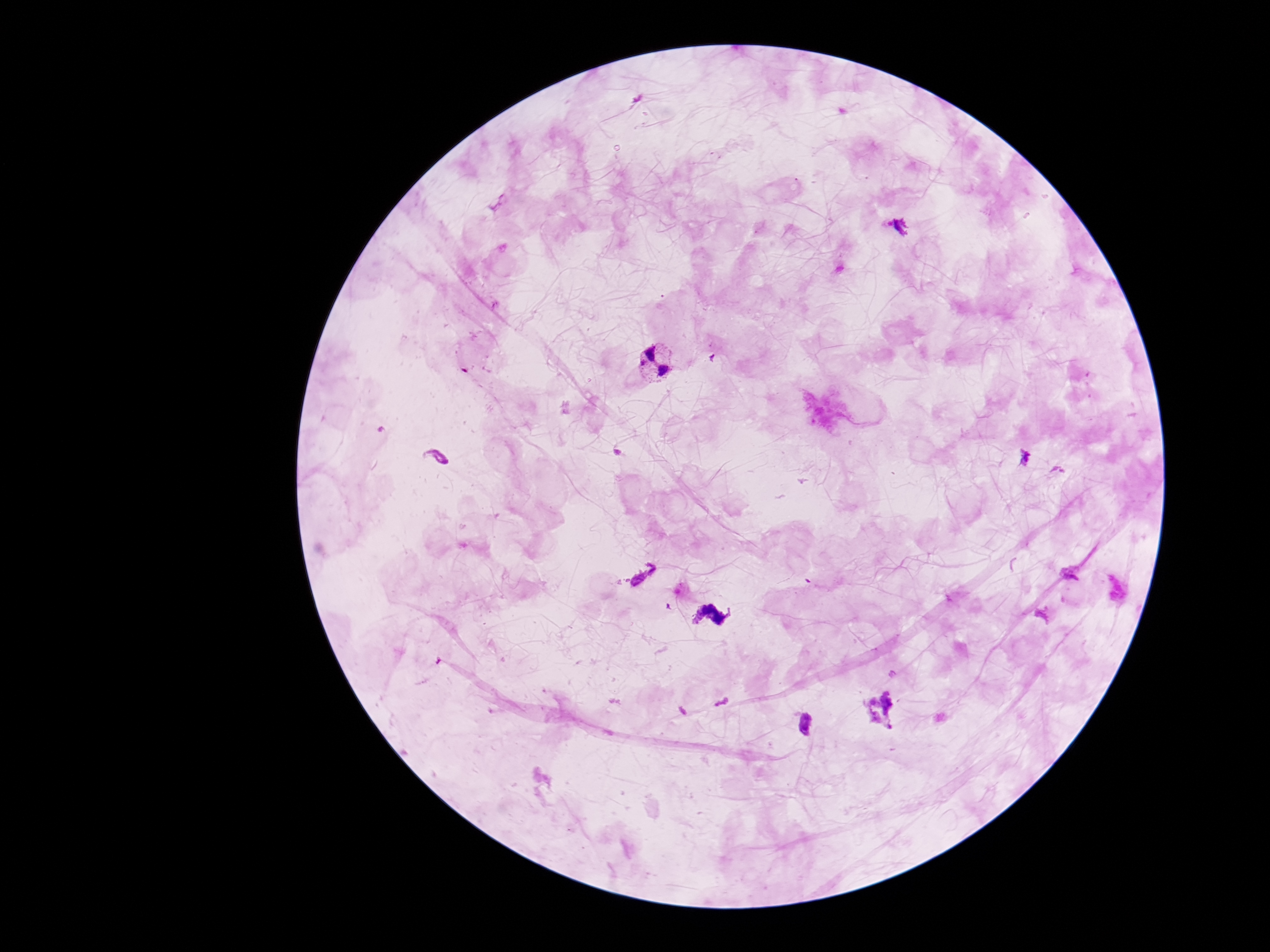

field of view = one from this slide
Plasmodium parasite locations = approximate object centers, in pixels from the top-left corner: (x=654, y=364), (x=643, y=575), (x=712, y=615)
stain = Giemsa
magnification = 100x
capture = smartphone camera through the microscope eyepiece
patient malaria status = infected
preparation = thick peripheral-blood smear
image size = 1270×952 pixels